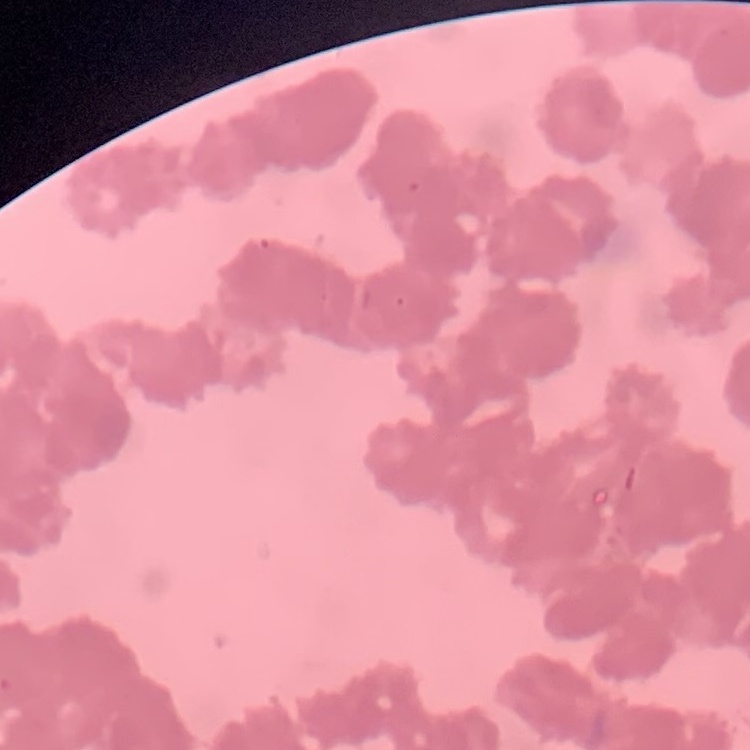

The erythrocytes show rouleaux formation. Stained with either Field's or Giemsa. Thin blood smear. Square crop of a larger photomicrograph.